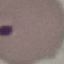

Summary:
  - Malaria status: uninfected
  - Stain: Giemsa
  - Preparation: thin smear
  - Capture: smartphone camera at the microscope eyepiece
  - Image type: automatically extracted cell patch, resized to 64 × 64 pixels